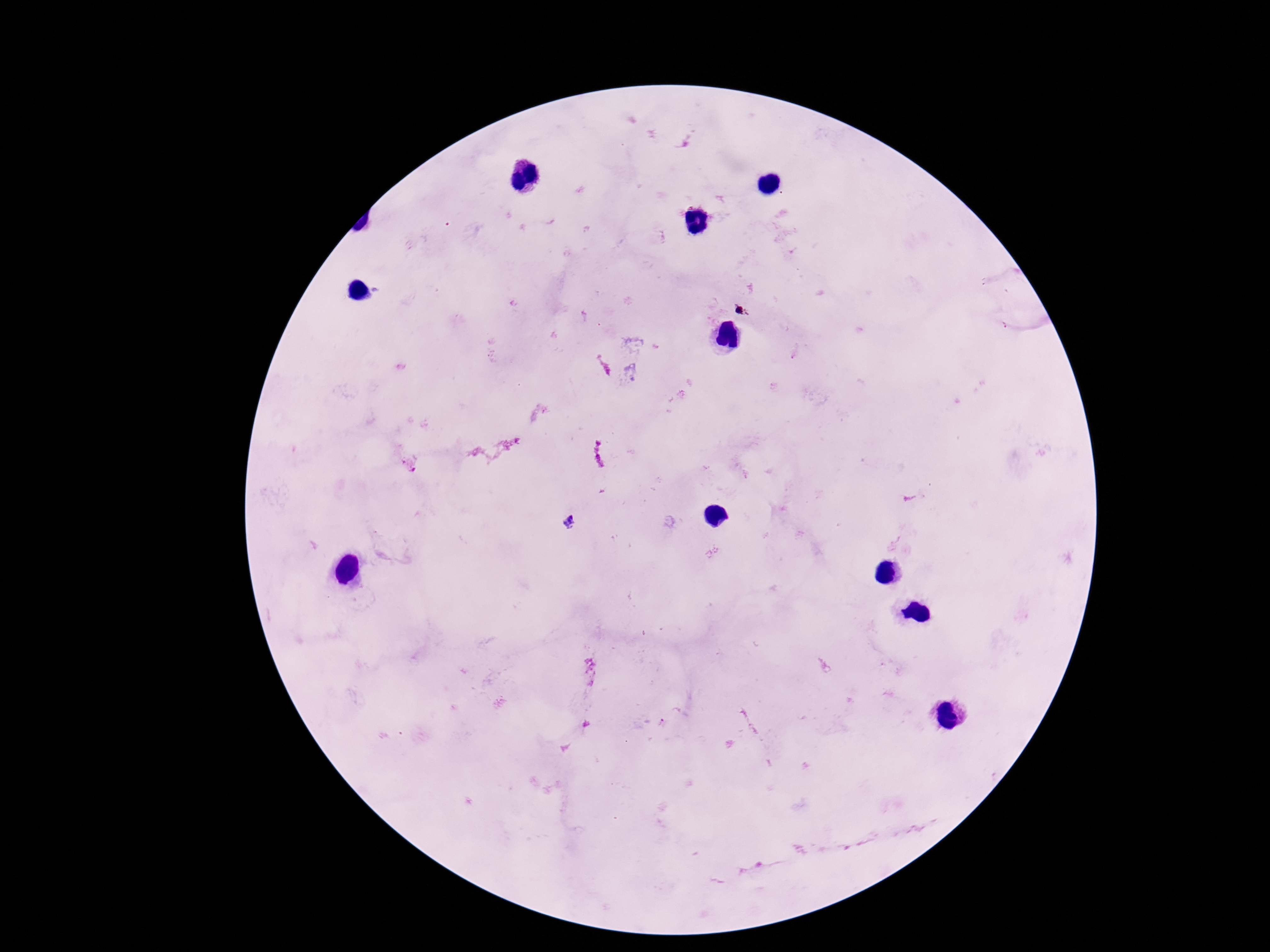
patient malaria status = positive
preparation = thick blood smear
capture = smartphone camera through the microscope eyepiece
image size = 1270×952 pixels
Plasmodium parasite locations = approximate centers as {x, y} in pixels: {411, 466}, {569, 522}
magnification = 100x
stain = Giemsa
field of view = single